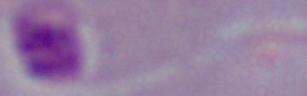

magnification = 1000x
identification = Leishmania
modality = micrograph